Report the malaria status of this cell.
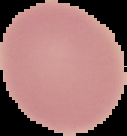

It is uninfected.

Summary:
  - Preparation: thin blood film
  - Image type: segmented cell region on a black background
  - Image size: 127×136 pixels